Identify the blood parasite species.
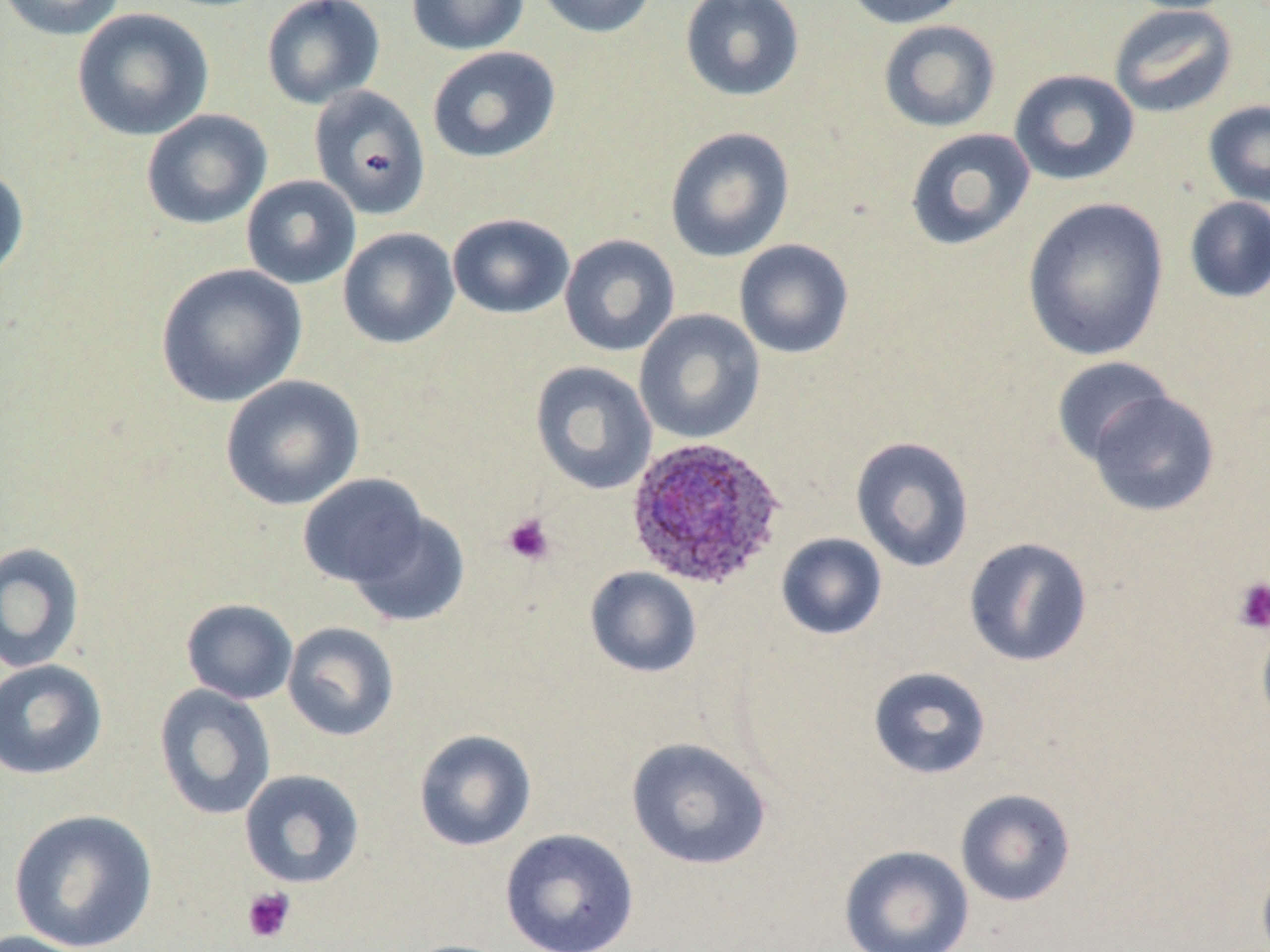
Plasmodium ovale.

{
  "preparation": "thin blood film",
  "stain": "May-Grünwald-Giemsa",
  "uninfected_red_blood_cell_locations": "approximate bounding boxes as (x1,y1)-(x2,y2) corner pairs in pixels: (1,0)-(126,41), (261,0)-(385,109), (406,0)-(529,56), (533,0)-(660,39), (679,0)-(805,102), (841,0)-(974,29), (1120,0)-(1241,14), (1107,3)-(1238,119), (72,8)-(214,141), (877,19)-(1001,133), (427,46)-(561,163), (1009,68)-(1140,187), (308,85)-(431,219), (1202,99)-(1270,207), (141,109)-(272,230), (664,126)-(795,263), (904,127)-(1036,251), (0,164)-(30,282), (241,175)-(361,289), (1021,196)-(1170,362), (1183,197)-(1270,303), (447,212)-(575,319), (337,227)-(460,349), (559,234)-(680,357), (734,239)-(854,359), (155,263)-(307,408), (634,309)-(765,444), (1051,356)-(1175,466), (529,361)-(657,495), (219,374)-(364,511), (1085,389)-(1221,517), (850,436)-(975,573), (299,474)-(429,589), (346,509)-(471,628), (776,533)-(888,641), (963,537)-(1093,667), (0,542)-(85,673), (584,566)-(702,678), (181,598)-(298,704), (1256,614)-(1270,735), (282,621)-(400,742), (0,659)-(108,780), (868,666)-(992,780), (153,684)-(276,821), (413,729)-(537,852), (625,737)-(772,871), (239,769)-(365,889), (954,788)-(1076,907), (8,808)-(158,952), (499,829)-(640,952), (838,844)-(975,952), (1256,856)-(1270,952), (1,930)-(100,952), (395,938)-(516,952)",
  "modality": "light microscopy",
  "plasmodium_ovale_infected_red_blood_cell_locations": "approximate bounding boxes as (x1,y1)-(x2,y2) corner pairs in pixels: (624,436)-(787,591)",
  "image_size": "1270×952 pixels",
  "magnification": "1000x",
  "platelet_locations": "approximate bounding boxes as (x1,y1)-(x2,y2) corner pairs in pixels: (502,513)-(555,566), (1233,576)-(1270,634), (242,887)-(296,943)",
  "field_of_view": "single"
}